Assess this cell for malaria.
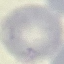
Uninfected.

Summary:
  - Image type: automatically extracted cell patch, resized to 64 × 64 pixels
  - Preparation: thin blood film
  - Capture: smartphone through the microscope eyepiece
  - Stain: Giemsa